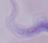

Photomicrograph. A trypanosome is shown. Captured at 1000x magnification.